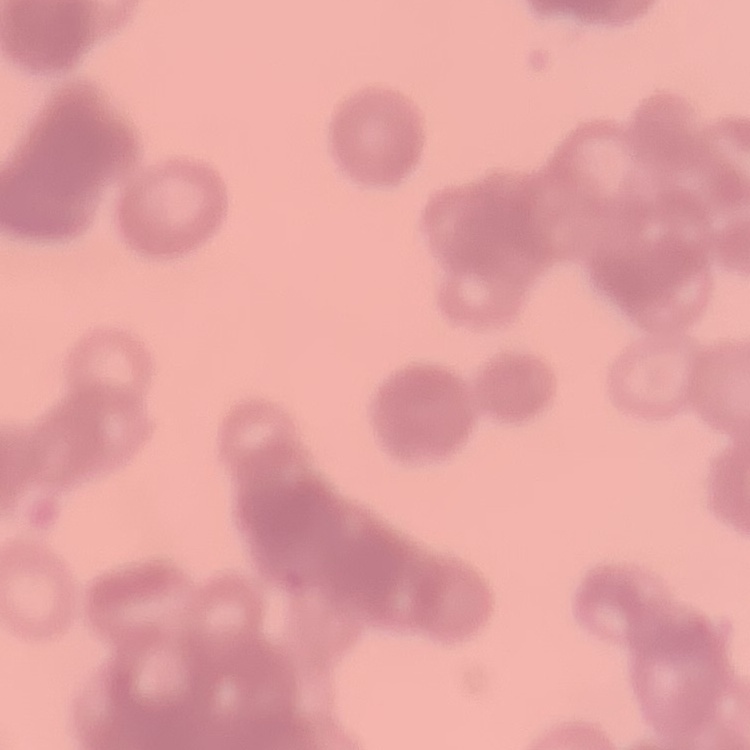

{
  "red_blood_cell_morphology": "rouleaux formation",
  "stain": "Field's or Giemsa",
  "image_type": "one tile cut from a larger photomicrograph",
  "preparation": "thin peripheral smear"
}